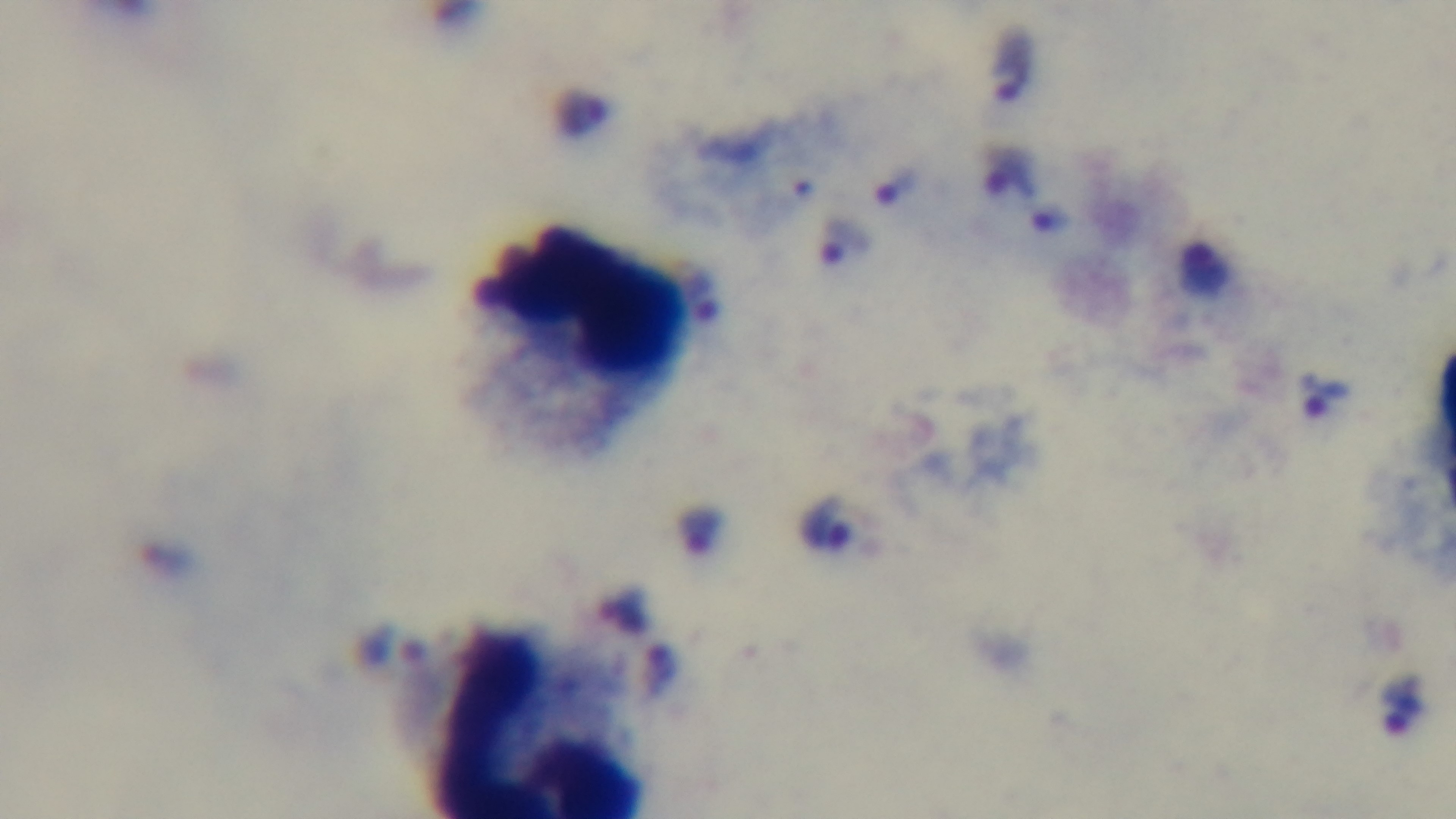

preparation = thick blood film
stain = Giemsa
malaria status = infected
capture = mounted 4K digital camera
modality = light microscopy
field of view = one from the slide
objective = 100x oil immersion